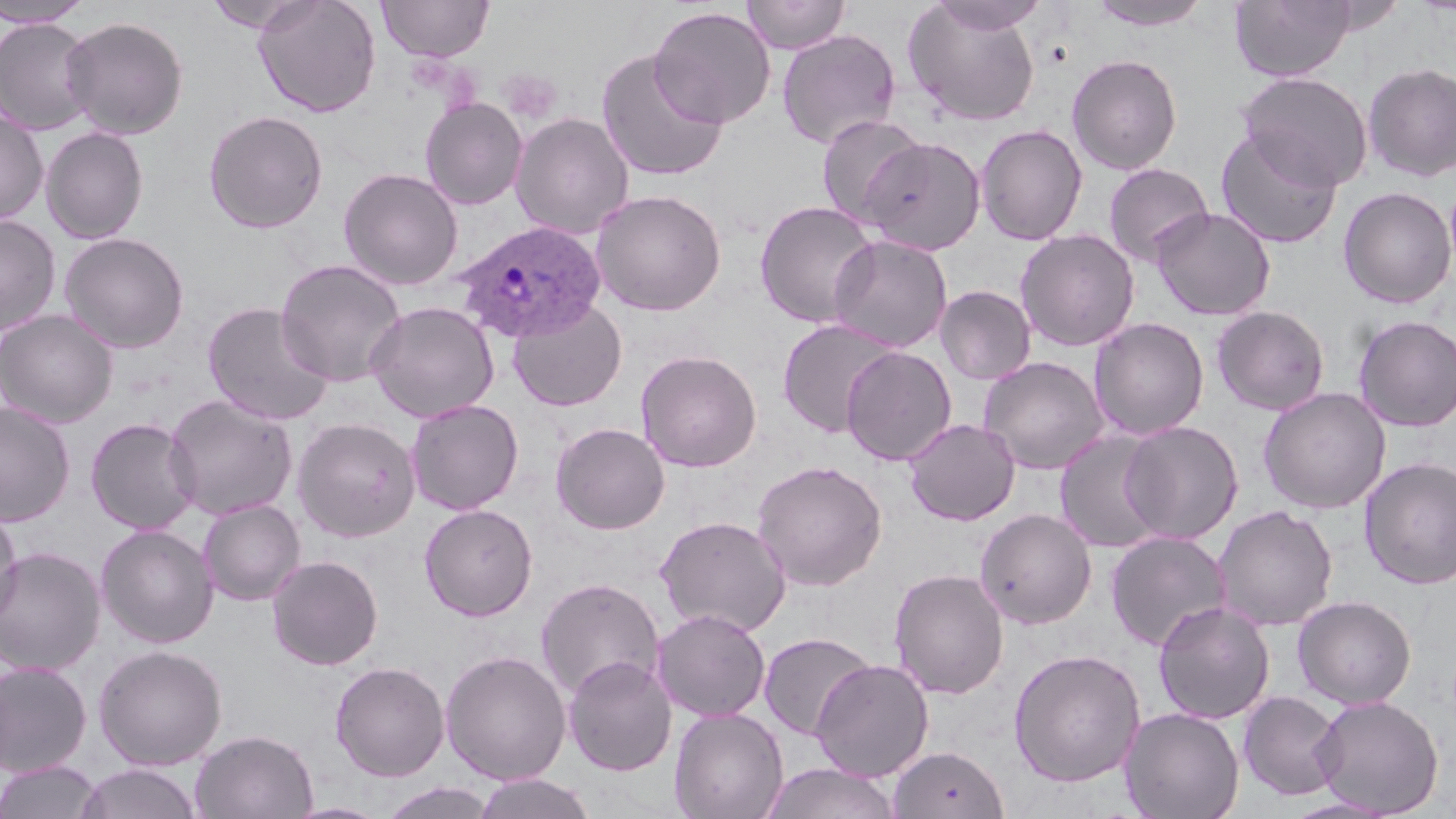 Approximate bounding boxes as (x1,y1)-(x2,y2) corner pairs in pixels. Plasmodium ovale-infected red blood cell locations: (453,220)-(607,342). Platelet locations: (499,69)-(561,122). Uninfected red blood cell locations: (204,0)-(316,32), (253,0)-(381,117), (378,0)-(494,61), (741,0)-(850,54), (927,0)-(1050,35), (1086,0)-(1213,31), (1229,0)-(1357,82), (0,1)-(93,27), (903,2)-(1042,127), (649,6)-(776,128), (61,16)-(189,140), (0,18)-(97,135), (777,29)-(901,150), (595,49)-(728,182), (1067,54)-(1182,175), (1362,62)-(1456,181), (1238,72)-(1373,190), (420,96)-(527,210), (0,109)-(48,225), (204,110)-(328,233), (510,112)-(634,240), (816,114)-(927,227), (975,123)-(1088,245), (41,127)-(149,244), (1215,127)-(1343,249), (858,136)-(987,255), (1103,162)-(1215,267), (338,167)-(463,290), (1338,186)-(1456,309), (590,189)-(727,316), (754,200)-(880,328), (1151,207)-(1275,320), (0,214)-(61,335), (1014,229)-(1140,352), (59,232)-(190,354), (827,235)-(952,353), (274,258)-(407,387), (935,286)-(1036,385), (507,296)-(627,412), (201,301)-(336,426), (365,301)-(500,423), (1211,305)-(1329,416), (0,309)-(118,428), (1352,315)-(1456,432), (777,317)-(903,439), (1089,317)-(1209,441), (841,346)-(957,466), (635,349)-(762,472), (978,356)-(1110,475), (1258,387)-(1391,514), (163,395)-(298,521), (406,399)-(524,515), (0,402)-(75,526), (85,417)-(201,535), (292,417)-(421,542), (902,418)-(1020,526), (1120,421)-(1243,544), (551,422)-(670,535), (1054,431)-(1169,554), (1359,457)-(1456,590), (751,459)-(888,591), (198,499)-(306,605), (420,504)-(538,620), (1212,505)-(1338,631), (0,506)-(23,628), (975,508)-(1097,629), (654,515)-(792,637), (96,524)-(218,648), (1105,531)-(1231,652), (0,547)-(106,675), (266,555)-(383,670), (888,568)-(1009,699), (535,577)-(665,701), (1293,595)-(1416,708), (1153,600)-(1275,724), (651,608)-(771,721), (758,632)-(877,741), (93,644)-(227,770), (1008,648)-(1145,786), (440,649)-(572,785), (563,655)-(676,776), (810,659)-(934,782), (0,661)-(93,777), (330,661)-(450,781), (1238,691)-(1345,800), (1311,695)-(1444,817), (669,707)-(789,819), (1120,707)-(1245,819), (191,729)-(318,818), (888,745)-(1010,819), (0,761)-(103,819), (761,763)-(902,819), (74,764)-(204,819), (472,773)-(596,819), (378,781)-(499,819), (1282,796)-(1399,818). Slide-level diagnosis: Plasmodium ovale. Thin blood smear. Image is 1456×819 pixels. May-Grünwald-Giemsa stain. Single field of view. Captured at 1000x magnification. Light microscopy.